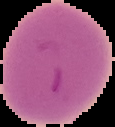
preparation = thin blood film
image type = segmented cell region with the area outside set to black
result = negative for Plasmodium parasites
image size = 115×127 pixels